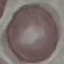

Summary:
  - Malaria status: uninfected
  - Stain: Giemsa
  - Image type: automatically extracted cell patch, resized to 64 × 64 pixels
  - Capture: smartphone camera at the microscope eyepiece
  - Preparation: thin blood smear